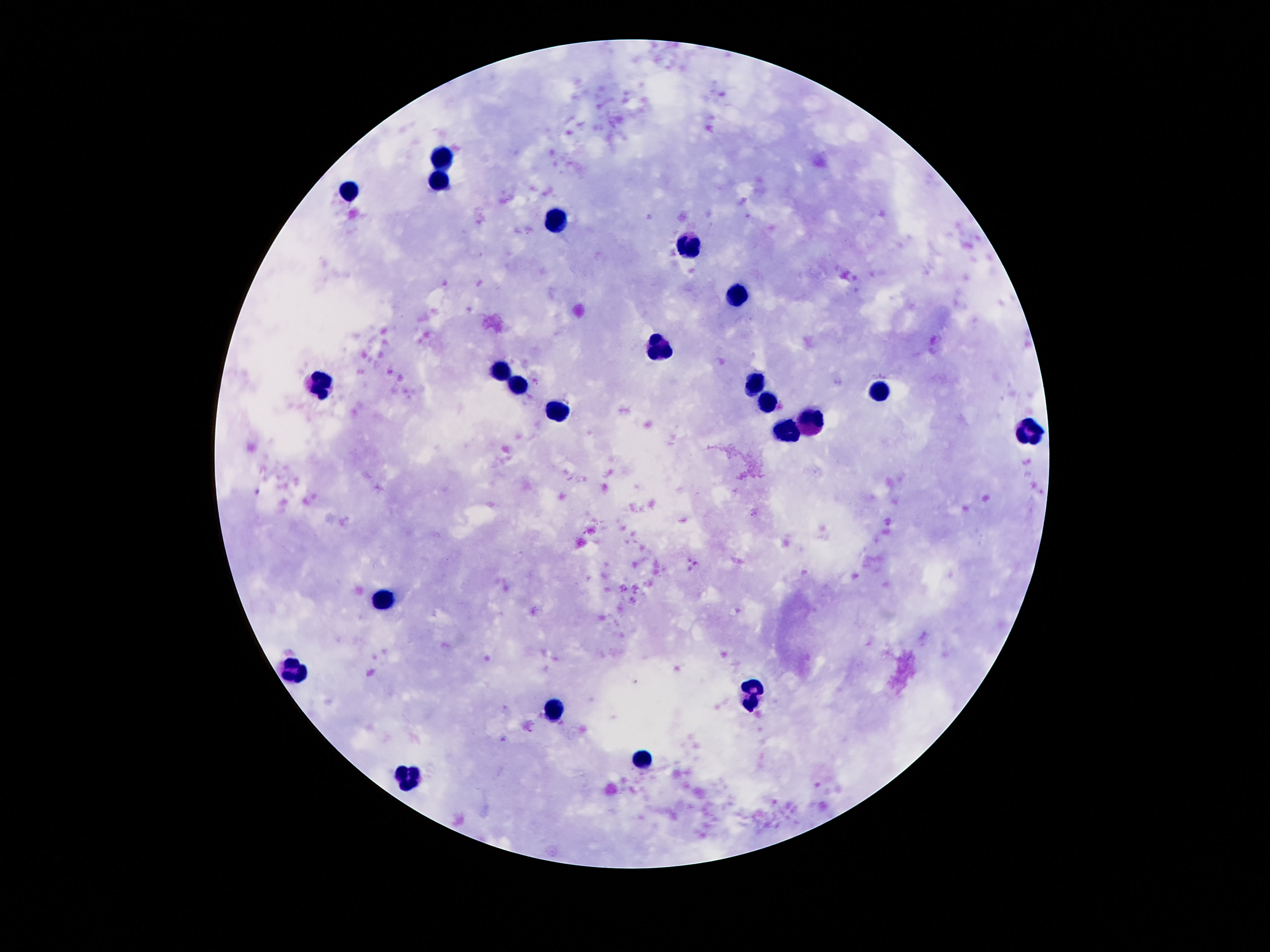 Approximate centers as (x, y) in pixels. Leukocyte locations: (444, 157), (439, 178), (350, 191), (558, 224), (693, 245), (737, 296), (661, 346), (500, 369), (322, 384), (516, 384), (759, 384), (882, 390), (770, 402), (554, 414), (811, 422), (787, 430), (1029, 433), (384, 598), (296, 670), (750, 696), (553, 708), (645, 760), (408, 773). Thick blood smear. Image is 1270×952 pixels. Photographed through the microscope eyepiece with a smartphone camera. 100x magnification. Patient malaria status: not infected. Giemsa-stained preparation. Single field of view.